Point out malaria parasites and leukocytes.
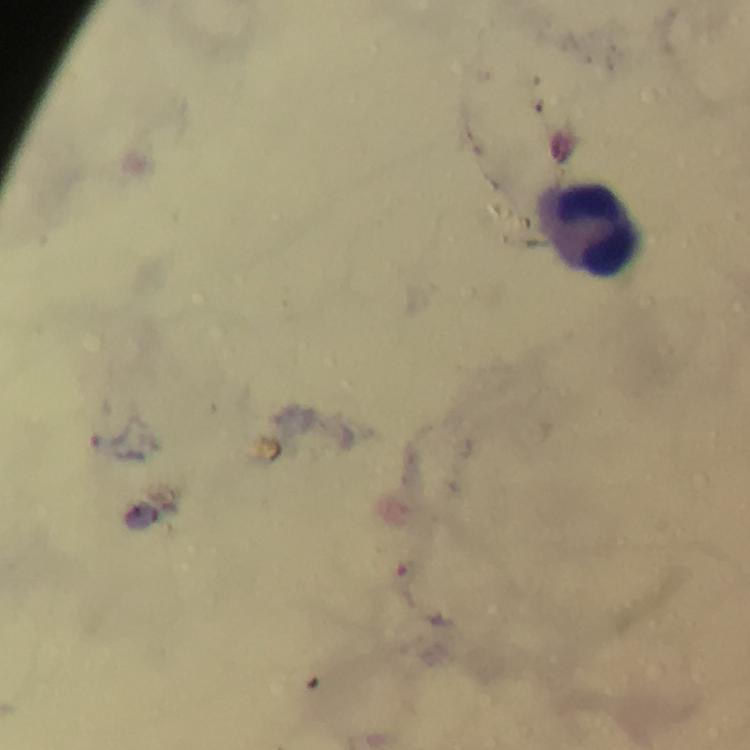
Approximate centers as {x, y} in pixels.
Malaria parasites: {406, 572}.
Leukocytes: {589, 224}.

100x magnification. Photographed with a smartphone mounted on the microscope. Giemsa-stained preparation. Thick blood smear. Immersion oil was used. Image is 750×750 pixels. A crop from one field of view. From a diagnostic examination for malaria.